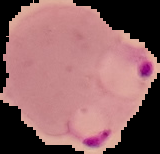

image_size: 160×154 pixels
preparation: thin blood film
malaria_status: parasitized
image_type: cell region segmented out of the field of view; surrounding area masked to black